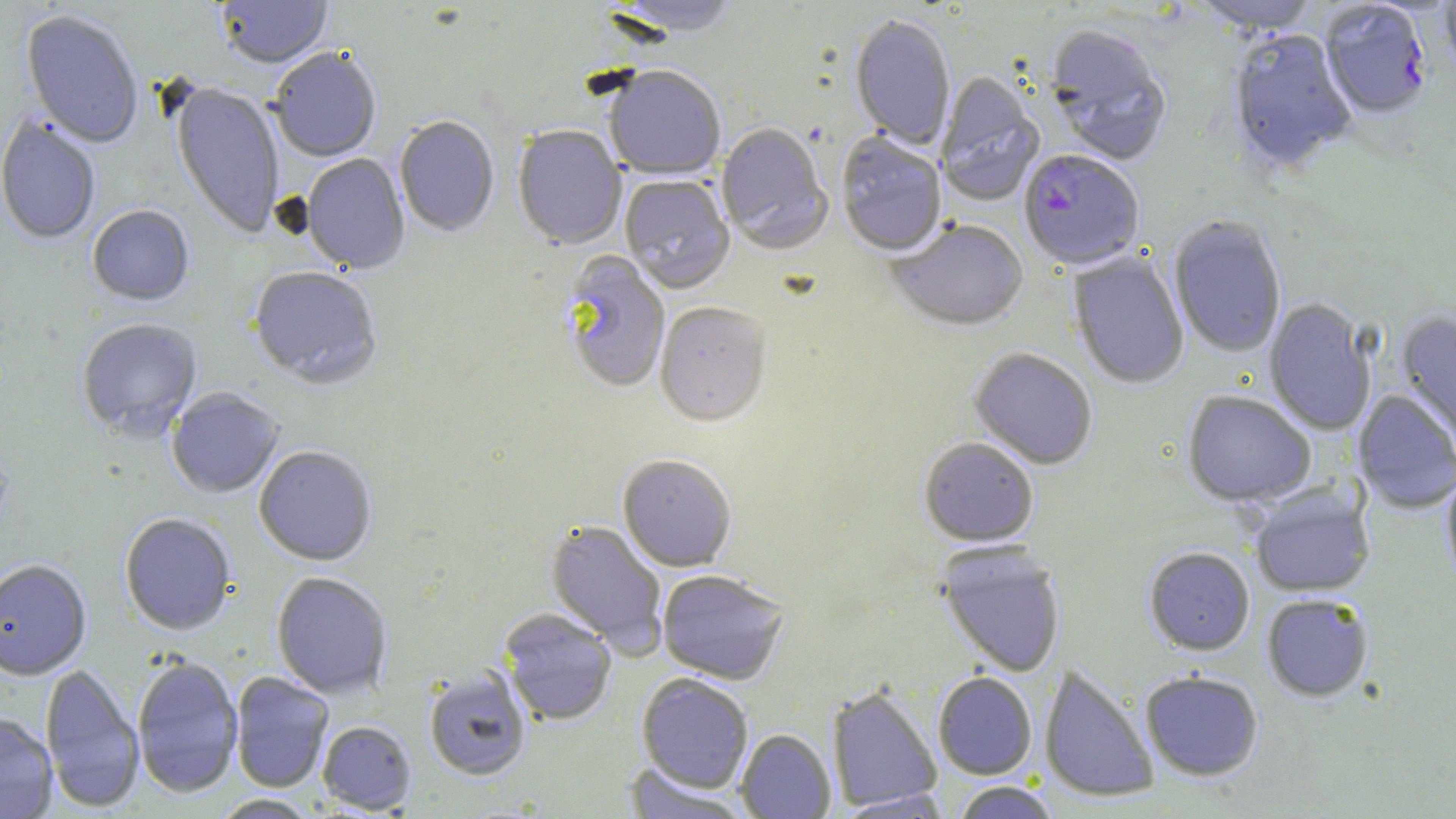

Approximate bounding boxes as (x1,y1)-(x2,y2) corner pairs in pixels. Plasmodium falciparum-infected red blood cell locations: (1318,2)-(1432,122), (1019,152)-(1144,271). Uninfected red blood cell locations: (217,0)-(333,71), (608,0)-(740,40), (1191,0)-(1320,37), (1437,0)-(1456,83), (21,11)-(143,150), (849,17)-(955,151), (1045,28)-(1172,168), (1229,31)-(1358,176), (270,50)-(381,164), (604,69)-(725,182), (935,72)-(1046,207), (170,84)-(284,239), (0,117)-(101,245), (394,117)-(499,238), (716,125)-(833,255), (513,126)-(627,251), (836,133)-(947,258), (300,155)-(410,276), (620,176)-(735,295), (87,207)-(194,307), (1169,217)-(1286,358), (887,220)-(1029,332), (1067,252)-(1189,390), (560,253)-(670,394), (248,269)-(382,390), (1263,299)-(1377,436), (655,304)-(771,429), (1396,310)-(1456,450), (76,320)-(202,442), (968,348)-(1097,471), (167,388)-(284,499), (1353,389)-(1456,514), (1182,391)-(1316,508), (918,438)-(1039,547), (254,447)-(377,566), (618,456)-(737,573), (1442,465)-(1456,592), (1249,485)-(1375,597), (119,514)-(236,636), (545,520)-(668,655), (937,544)-(1066,677), (1144,547)-(1255,656), (0,561)-(92,681), (657,571)-(788,685), (272,572)-(391,700), (1262,594)-(1375,703), (499,609)-(616,725), (132,657)-(244,799), (40,664)-(145,812), (1039,664)-(1159,803), (424,668)-(531,781), (1140,670)-(1263,781), (230,672)-(334,793), (933,672)-(1037,779), (636,674)-(753,793), (827,685)-(942,812), (0,713)-(58,819), (318,721)-(416,814), (736,729)-(836,818), (623,763)-(749,819), (950,781)-(1061,819), (834,790)-(952,817), (211,794)-(319,818). Slide-level diagnosis: Plasmodium falciparum. Single field of view. Thin blood film. May-Grünwald-Giemsa stain. Optical microscopy. Image is 1456×819 pixels. Captured at 1000x magnification.